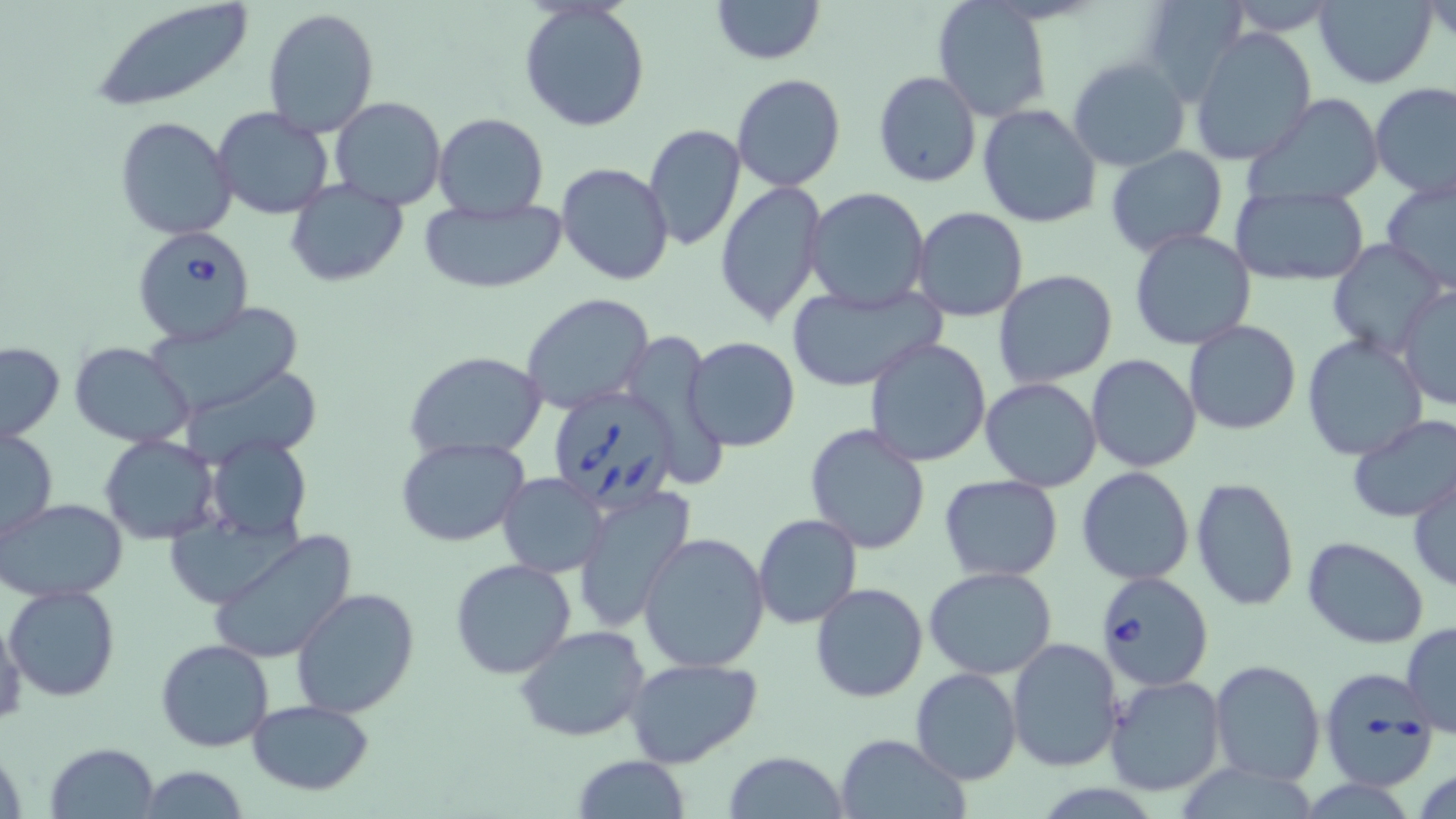
Approximate bounding boxes as (x1, y1, x2, y2) in pixels. Uninfected red blood cell locations: (712, 0, 824, 65), (1136, 0, 1245, 103), (1314, 0, 1437, 88), (88, 1, 258, 110), (519, 2, 651, 133), (933, 2, 1052, 120), (261, 7, 379, 136), (1190, 28, 1316, 164), (1068, 56, 1191, 172), (872, 71, 982, 188), (731, 73, 846, 191), (871, 82, 1089, 200), (1370, 83, 1456, 199), (1249, 93, 1385, 205), (329, 96, 447, 210), (977, 103, 1104, 230), (212, 107, 335, 220), (433, 113, 548, 220), (114, 116, 238, 240), (643, 124, 746, 252), (1104, 148, 1228, 257), (556, 162, 672, 285), (716, 179, 827, 325), (286, 180, 410, 287), (1379, 182, 1456, 296), (804, 187, 932, 312), (1231, 188, 1369, 286), (420, 198, 566, 294), (911, 206, 1029, 322), (1129, 228, 1256, 349), (1327, 237, 1448, 359), (992, 270, 1118, 389), (785, 281, 944, 395), (1396, 287, 1456, 408), (521, 292, 656, 413), (144, 301, 307, 415), (1185, 322, 1300, 436), (1302, 335, 1428, 462), (684, 336, 801, 453), (864, 336, 993, 466), (0, 341, 65, 443), (69, 341, 195, 448), (404, 351, 548, 460), (1086, 354, 1202, 472), (980, 377, 1104, 492), (1347, 415, 1456, 524), (803, 424, 932, 555), (0, 426, 58, 542), (100, 435, 221, 544), (205, 435, 312, 544), (397, 436, 529, 546), (1077, 467, 1196, 585), (498, 472, 608, 578), (1409, 472, 1456, 592), (939, 474, 1065, 582), (1192, 477, 1299, 611), (573, 487, 697, 630), (1, 498, 129, 601), (753, 513, 861, 628), (207, 529, 360, 665), (638, 531, 770, 671), (1301, 536, 1429, 648), (450, 558, 577, 679), (924, 566, 1060, 678), (810, 582, 929, 701), (5, 585, 120, 700), (291, 588, 419, 717), (0, 613, 27, 722), (1401, 623, 1455, 737), (514, 625, 651, 744), (1007, 638, 1125, 773), (155, 639, 273, 752), (624, 657, 766, 770), (1209, 660, 1325, 785), (910, 668, 1024, 785), (1103, 674, 1226, 796), (247, 700, 376, 795), (833, 733, 968, 818), (48, 742, 159, 818), (724, 751, 849, 819), (571, 755, 692, 818), (134, 765, 251, 818). Babesia divergens-infected red blood cell locations: (131, 226, 255, 343), (546, 386, 683, 512), (1096, 570, 1214, 694), (1316, 669, 1436, 791). Slide-level diagnosis: Babesia divergens. Optical microscopy. May-Grünwald-Giemsa-stained preparation. Image is 1456×819 pixels. One field of a larger specimen. Captured at 1000x magnification. Thin blood smear.